Identify the parasite.
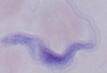

A trypanosome.

Summary:
  - Magnification: 1000x
  - Modality: micrograph